Report the malaria status of this cell.
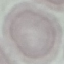
Uninfected.

Summary:
  - Capture: smartphone through the microscope eyepiece
  - Stain: Giemsa
  - Image type: automatically extracted cell patch, resized to 64 × 64 pixels
  - Preparation: thin blood film